Assess this cell for malaria.
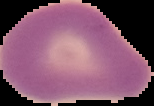

Uninfected.

image_type: segmented cell region on a black background
preparation: thin blood film
image_size: 154×106 pixels